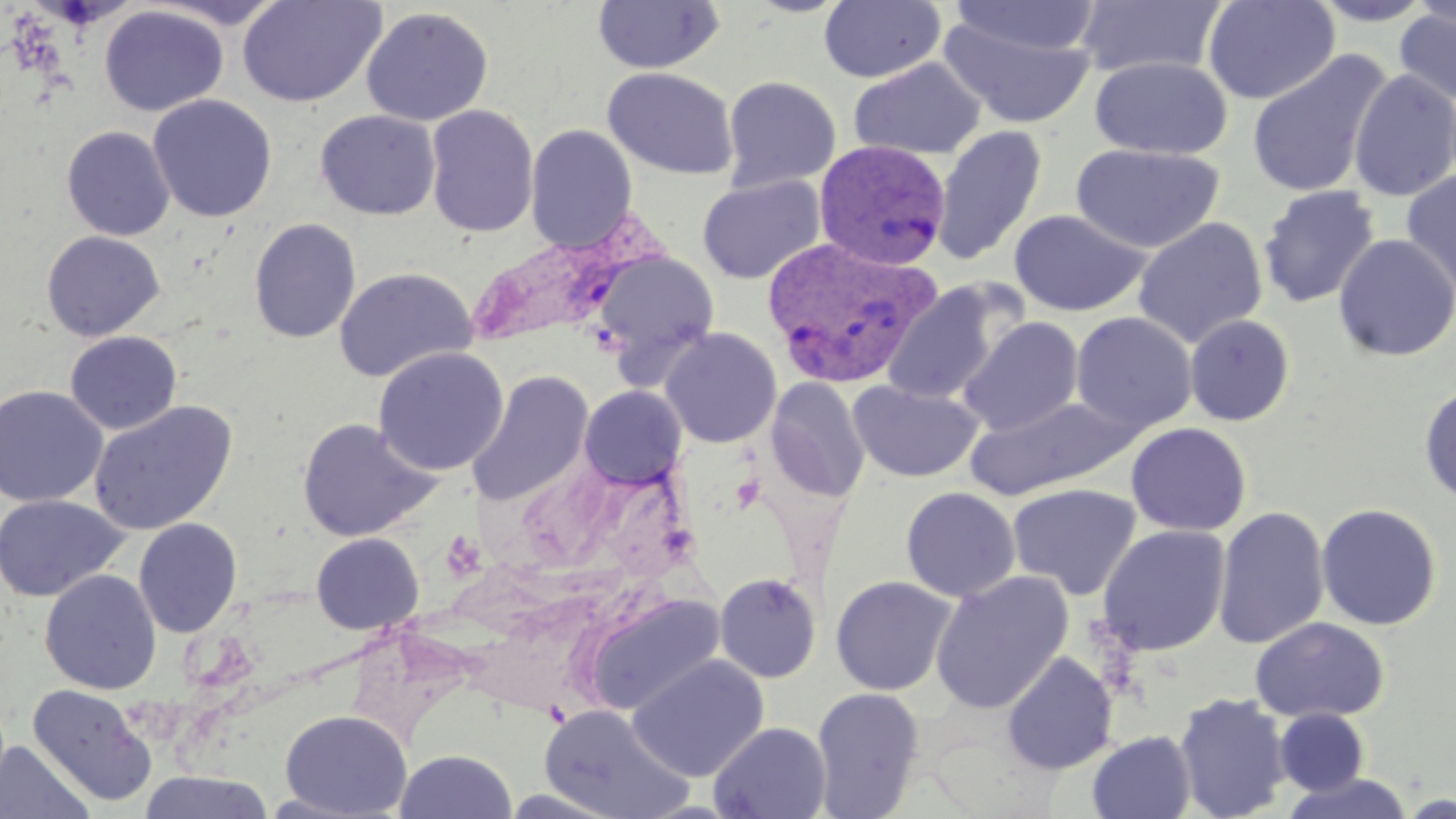

Summary:
  - Coordinate format: approximate bounding boxes as (x1,y1)-(x2,y2) corner pairs in pixels
  - Plasmodium vivax-infected red blood cell locations: (814,140)-(951,270), (465,228)-(639,347), (761,235)-(943,387)
  - Uninfected red blood cell locations: (236,0)-(387,108), (592,0)-(725,75), (1202,0)-(1340,105), (1309,0)-(1435,26), (1408,0)-(1456,29), (143,1)-(292,30), (819,1)-(946,84), (947,1)-(1102,59), (1072,1)-(1228,79), (99,4)-(228,117), (1394,5)-(1456,107), (360,6)-(494,127), (938,11)-(1098,130), (1246,49)-(1391,199), (1090,55)-(1232,159), (848,57)-(987,161), (602,67)-(739,180), (1348,69)-(1456,201), (721,75)-(841,192), (147,94)-(278,222), (424,105)-(539,238), (315,110)-(441,220), (524,124)-(637,252), (931,124)-(1047,266), (61,126)-(175,241), (1069,142)-(1226,254), (1400,169)-(1456,300), (697,175)-(826,284), (1257,185)-(1380,309), (1009,209)-(1150,316), (1132,217)-(1268,348), (248,218)-(361,343), (41,231)-(165,341), (1333,234)-(1456,361), (591,251)-(720,373), (334,267)-(477,382), (881,281)-(1014,406), (1070,312)-(1197,434), (1184,314)-(1295,426), (957,316)-(1084,436), (660,327)-(782,448), (64,331)-(183,435), (373,346)-(509,476), (467,370)-(594,506), (765,377)-(870,502), (849,380)-(984,482), (1418,383)-(1456,506), (0,385)-(108,507), (579,385)-(687,489), (964,395)-(1138,500), (88,401)-(238,536), (296,417)-(440,542), (1125,422)-(1251,536), (1007,483)-(1142,600), (900,487)-(1021,602), (0,493)-(128,603), (1315,503)-(1442,631), (1213,505)-(1330,650), (133,517)-(242,638), (1097,524)-(1231,655), (311,532)-(424,635), (40,569)-(161,695), (929,570)-(1074,714), (714,572)-(822,682), (830,575)-(958,696), (578,592)-(727,716), (1250,617)-(1390,723), (1002,651)-(1118,774), (627,654)-(770,781), (27,684)-(158,808), (810,687)-(925,818), (1174,692)-(1291,819), (540,704)-(692,819), (279,709)-(412,818), (1274,709)-(1369,794), (709,722)-(832,819), (1087,730)-(1196,819), (0,740)-(95,819), (394,748)-(518,818), (137,770)-(276,818), (1280,772)-(1415,818)
  - Slide-level diagnosis: Plasmodium vivax
  - Preparation: thin blood smear
  - Magnification: 1000x
  - Modality: optical microscopy
  - Image size: 1456×819 pixels
  - Stain: May-Grünwald-Giemsa
  - Field of view: single